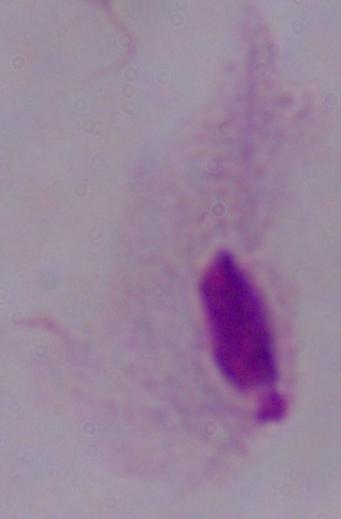
Summary:
  - Identification: trichomonad
  - Magnification: 1000x
  - Modality: photomicrograph